Describe the morphology of the red blood cells.
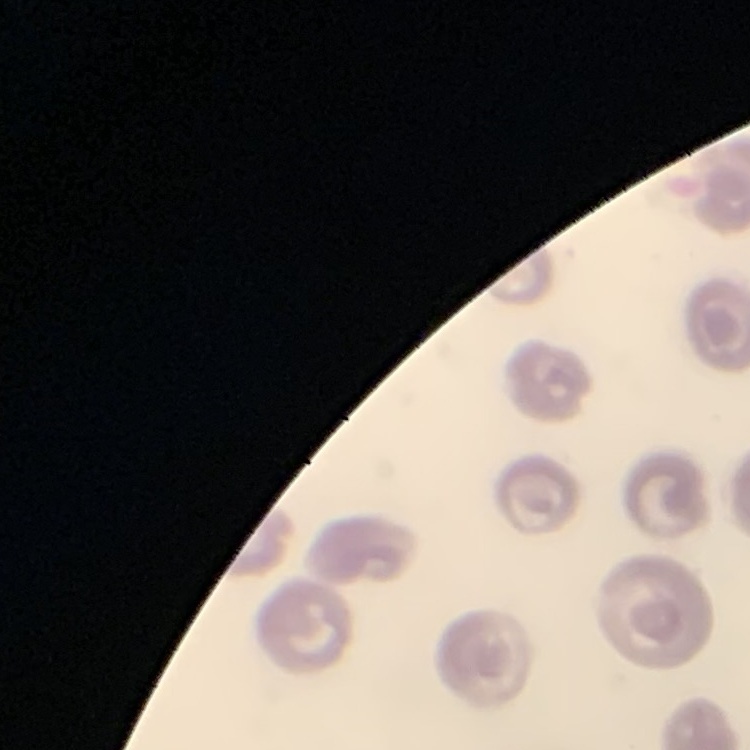

No rouleaux formation.

image type = one tile cut from a larger photomicrograph
preparation = thin blood smear
stain = Field's or Giemsa